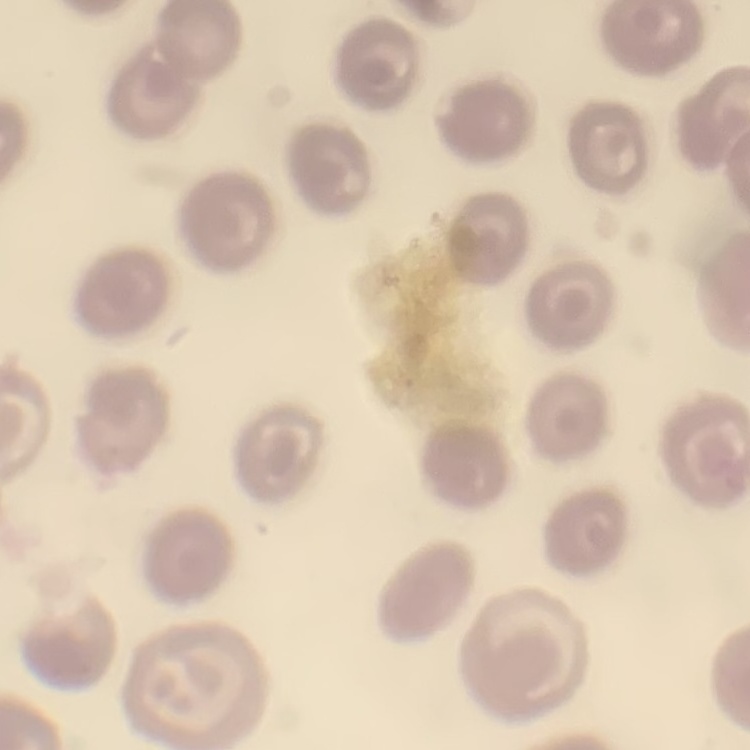

Summary:
  - Red blood cell morphology: no rouleaux formation
  - Image type: square crop of a larger photomicrograph
  - Stain: Field's or Giemsa
  - Preparation: thin blood smear